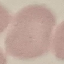
Summary:
  - Result: no malaria parasites detected
  - Stain: Giemsa
  - Capture: smartphone through the microscope eyepiece
  - Preparation: thin blood film
  - Image type: cell patch, automatically extracted from a larger field of view and resized to 64 × 64 pixels